Identify the cell.
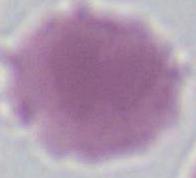

This is an erythrocyte.

Summary:
  - Modality: photomicrograph
  - Magnification: 1000x